Assess this cell for malaria.
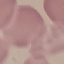

Uninfected.

Summary:
  - Capture: smartphone camera at the microscope eyepiece
  - Stain: Giemsa
  - Image type: automatically extracted cell patch, resized to 64 × 64 pixels
  - Preparation: thin blood film